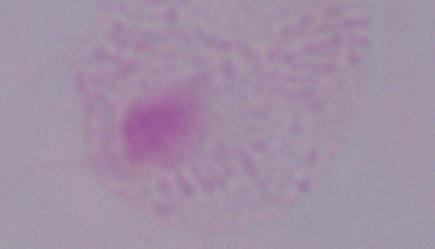

A trichomonad is seen. 1000x magnification. Photomicrograph.